State which parasite is depicted.
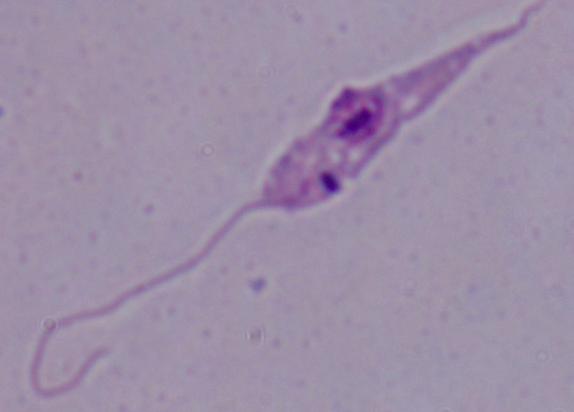

This is Leishmania.

modality = micrograph
magnification = 1000x